Locate every uninfected red blood cell.
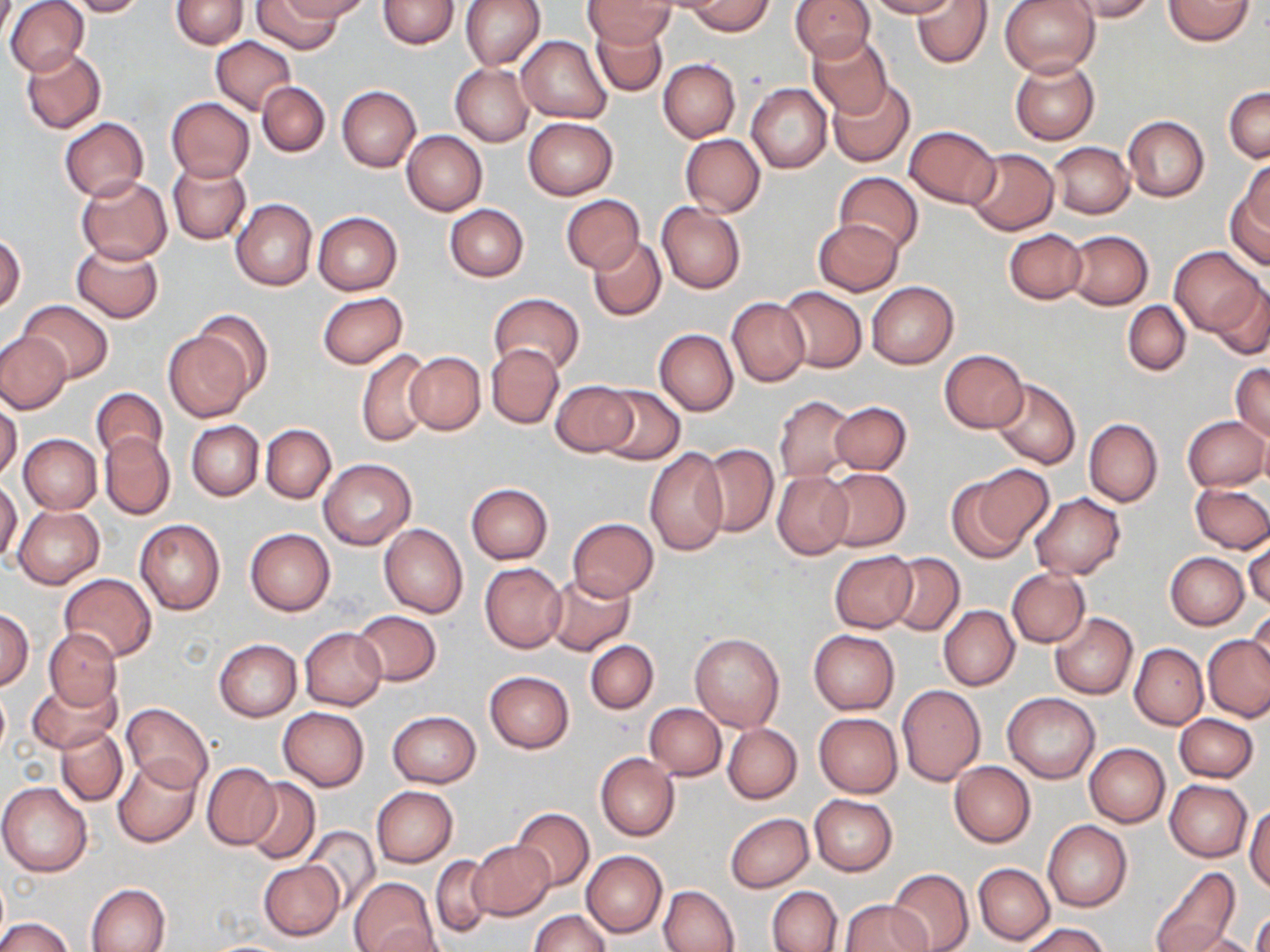
Approximate bounding boxes as named x1/y1/x2/y2 corners in pixels.
Uninfected red blood cells: (x1=5, y1=0, x2=88, y2=77), (x1=65, y1=0, x2=144, y2=16), (x1=171, y1=0, x2=248, y2=49), (x1=252, y1=0, x2=344, y2=54), (x1=280, y1=0, x2=369, y2=22), (x1=376, y1=0, x2=459, y2=48), (x1=460, y1=0, x2=545, y2=70), (x1=789, y1=0, x2=875, y2=61), (x1=866, y1=0, x2=957, y2=19), (x1=913, y1=0, x2=991, y2=69), (x1=999, y1=0, x2=1100, y2=77), (x1=1063, y1=0, x2=1157, y2=22), (x1=1164, y1=0, x2=1254, y2=43), (x1=582, y1=1, x2=678, y2=47), (x1=687, y1=1, x2=773, y2=35), (x1=590, y1=18, x2=668, y2=97), (x1=806, y1=33, x2=892, y2=118), (x1=516, y1=35, x2=612, y2=123), (x1=212, y1=36, x2=296, y2=115), (x1=21, y1=47, x2=106, y2=133), (x1=658, y1=58, x2=741, y2=143), (x1=1009, y1=58, x2=1100, y2=144), (x1=451, y1=64, x2=534, y2=146), (x1=828, y1=79, x2=914, y2=167), (x1=257, y1=81, x2=330, y2=157), (x1=746, y1=84, x2=832, y2=173), (x1=337, y1=85, x2=421, y2=173), (x1=1224, y1=87, x2=1269, y2=162), (x1=166, y1=97, x2=254, y2=182), (x1=1123, y1=115, x2=1209, y2=201), (x1=523, y1=117, x2=617, y2=198), (x1=59, y1=118, x2=148, y2=201), (x1=903, y1=125, x2=1001, y2=208), (x1=402, y1=130, x2=487, y2=214), (x1=679, y1=133, x2=765, y2=217), (x1=1049, y1=142, x2=1133, y2=218), (x1=964, y1=149, x2=1059, y2=234), (x1=1240, y1=159, x2=1269, y2=235), (x1=168, y1=161, x2=250, y2=245), (x1=833, y1=171, x2=923, y2=254), (x1=75, y1=175, x2=172, y2=264), (x1=1227, y1=187, x2=1270, y2=270), (x1=561, y1=194, x2=645, y2=274), (x1=232, y1=199, x2=317, y2=291), (x1=657, y1=204, x2=746, y2=294), (x1=445, y1=205, x2=528, y2=281), (x1=312, y1=211, x2=402, y2=295), (x1=814, y1=218, x2=902, y2=295), (x1=1005, y1=228, x2=1087, y2=304), (x1=1065, y1=230, x2=1153, y2=309), (x1=1, y1=232, x2=26, y2=314), (x1=588, y1=237, x2=666, y2=322), (x1=71, y1=242, x2=164, y2=323), (x1=1172, y1=245, x2=1260, y2=334), (x1=1209, y1=278, x2=1270, y2=361), (x1=866, y1=280, x2=959, y2=369), (x1=779, y1=286, x2=867, y2=373), (x1=317, y1=292, x2=408, y2=369), (x1=489, y1=293, x2=584, y2=375), (x1=726, y1=297, x2=809, y2=386), (x1=17, y1=301, x2=113, y2=383), (x1=1123, y1=301, x2=1190, y2=375), (x1=188, y1=309, x2=275, y2=401), (x1=163, y1=326, x2=257, y2=422), (x1=654, y1=330, x2=737, y2=416), (x1=0, y1=333, x2=71, y2=413), (x1=487, y1=344, x2=564, y2=429), (x1=357, y1=349, x2=433, y2=447), (x1=940, y1=349, x2=1028, y2=432), (x1=404, y1=351, x2=485, y2=435), (x1=1230, y1=363, x2=1270, y2=442), (x1=549, y1=379, x2=636, y2=456), (x1=991, y1=379, x2=1080, y2=469), (x1=597, y1=386, x2=685, y2=465), (x1=92, y1=387, x2=167, y2=464), (x1=773, y1=396, x2=857, y2=481), (x1=0, y1=398, x2=22, y2=481), (x1=829, y1=401, x2=911, y2=474), (x1=1183, y1=416, x2=1268, y2=491), (x1=1084, y1=418, x2=1163, y2=507), (x1=188, y1=420, x2=263, y2=500), (x1=261, y1=424, x2=336, y2=502), (x1=1258, y1=427, x2=1270, y2=496), (x1=100, y1=433, x2=174, y2=519), (x1=19, y1=434, x2=101, y2=513), (x1=700, y1=444, x2=778, y2=536), (x1=645, y1=447, x2=729, y2=556), (x1=319, y1=459, x2=415, y2=550), (x1=957, y1=466, x2=1052, y2=556), (x1=820, y1=467, x2=911, y2=551), (x1=772, y1=470, x2=853, y2=560), (x1=0, y1=480, x2=22, y2=564), (x1=1190, y1=482, x2=1270, y2=553), (x1=466, y1=483, x2=552, y2=564), (x1=1029, y1=493, x2=1124, y2=579), (x1=14, y1=506, x2=104, y2=588), (x1=567, y1=518, x2=659, y2=600), (x1=135, y1=519, x2=225, y2=615), (x1=379, y1=523, x2=468, y2=618), (x1=245, y1=528, x2=334, y2=615), (x1=1244, y1=532, x2=1270, y2=611), (x1=829, y1=551, x2=917, y2=633), (x1=886, y1=553, x2=964, y2=635), (x1=1165, y1=553, x2=1249, y2=629), (x1=480, y1=562, x2=567, y2=653), (x1=1006, y1=568, x2=1090, y2=647), (x1=58, y1=574, x2=157, y2=661), (x1=544, y1=574, x2=635, y2=656), (x1=1247, y1=605, x2=1270, y2=688), (x1=939, y1=606, x2=1020, y2=690), (x1=0, y1=608, x2=34, y2=689), (x1=353, y1=610, x2=441, y2=686), (x1=1050, y1=613, x2=1138, y2=698), (x1=299, y1=627, x2=387, y2=710), (x1=44, y1=628, x2=121, y2=709), (x1=809, y1=629, x2=900, y2=714), (x1=690, y1=632, x2=783, y2=731), (x1=1204, y1=635, x2=1270, y2=722), (x1=214, y1=638, x2=302, y2=721), (x1=585, y1=640, x2=658, y2=714), (x1=1130, y1=643, x2=1207, y2=729), (x1=484, y1=671, x2=574, y2=753), (x1=29, y1=677, x2=120, y2=754), (x1=0, y1=684, x2=9, y2=760), (x1=897, y1=685, x2=985, y2=785), (x1=1003, y1=692, x2=1100, y2=783), (x1=120, y1=702, x2=213, y2=793), (x1=645, y1=703, x2=726, y2=779), (x1=278, y1=707, x2=369, y2=790), (x1=387, y1=711, x2=481, y2=788), (x1=815, y1=713, x2=903, y2=797), (x1=1174, y1=714, x2=1257, y2=782), (x1=724, y1=723, x2=801, y2=803), (x1=56, y1=727, x2=127, y2=805), (x1=1085, y1=744, x2=1169, y2=826), (x1=596, y1=753, x2=678, y2=841), (x1=113, y1=757, x2=200, y2=847), (x1=949, y1=761, x2=1035, y2=847), (x1=203, y1=763, x2=282, y2=850), (x1=244, y1=778, x2=320, y2=863), (x1=1166, y1=780, x2=1252, y2=861), (x1=0, y1=782, x2=91, y2=876), (x1=372, y1=786, x2=457, y2=867), (x1=810, y1=795, x2=897, y2=875), (x1=1245, y1=804, x2=1270, y2=894), (x1=511, y1=807, x2=594, y2=891), (x1=725, y1=813, x2=813, y2=892), (x1=1042, y1=819, x2=1132, y2=912), (x1=304, y1=827, x2=381, y2=910), (x1=469, y1=842, x2=553, y2=920), (x1=581, y1=850, x2=667, y2=937), (x1=432, y1=855, x2=493, y2=938), (x1=259, y1=860, x2=344, y2=941), (x1=973, y1=863, x2=1054, y2=944), (x1=1149, y1=867, x2=1238, y2=951), (x1=886, y1=868, x2=973, y2=952), (x1=349, y1=876, x2=438, y2=952), (x1=87, y1=883, x2=171, y2=952), (x1=659, y1=885, x2=738, y2=952), (x1=767, y1=886, x2=842, y2=952), (x1=840, y1=900, x2=930, y2=952), (x1=529, y1=909, x2=610, y2=952), (x1=1251, y1=910, x2=1270, y2=952), (x1=0, y1=916, x2=72, y2=952), (x1=1020, y1=922, x2=1107, y2=952), (x1=369, y1=925, x2=451, y2=952), (x1=1175, y1=931, x2=1263, y2=952).

Summary:
  - Slide-level diagnosis: no evidence of blood parasites
  - Field of view: single
  - Modality: light microscopy
  - Image size: 1270×952 pixels
  - Preparation: thin blood film
  - Stain: May-Grünwald-Giemsa
  - Magnification: 1000x